Assess this cell for malaria.
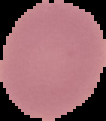
It is uninfected.

image size = 106×121 pixels
preparation = thin blood smear
image type = segmented cell region on a black background